Point out each malaria parasite.
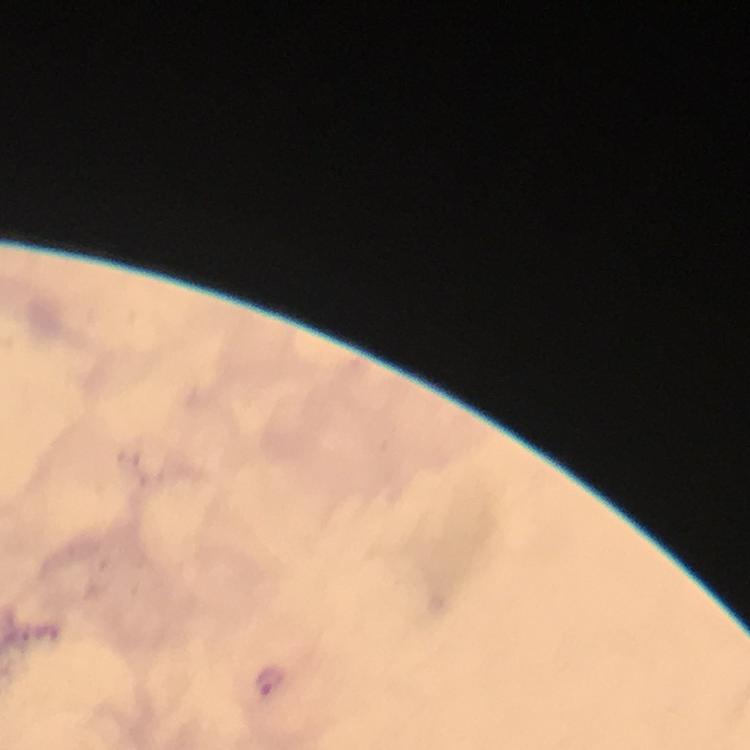
Approximate centers as {x, y} in pixels.
Malaria parasites: {274, 682}.

capture = smartphone photograph through a microscope
image size = 750×750 pixels
stain = Giemsa
context = from a malaria diagnostic workup
preparation = thick smear
immersion oil = used
cropped from = one field of view
magnification = 100x